Name the cell type shown.
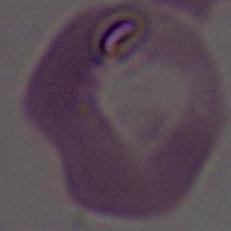
An erythrocyte.

Summary:
  - Modality: micrograph
  - Magnification: 1000x